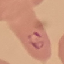 Malaria status: parasitized. Acquired by smartphone through the microscope eyepiece. Giemsa-stained preparation. Cell patch, automatically extracted from a larger field of view and resized to 64 × 64 pixels. Thin blood film.